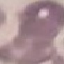

Result: negative for malaria parasites. Photographed with a smartphone camera at the microscope eyepiece. Giemsa-stained preparation. Cell patch, automatically extracted from a larger field of view and resized to 64 × 64 pixels. Thin smear of blood.